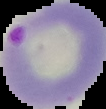

malaria status = parasitized
image size = 106×109 pixels
preparation = thin blood film
image type = cell region segmented out of the field of view; surrounding area masked to black